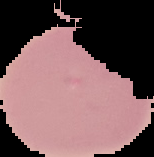
image size = 154×157 pixels
preparation = thin blood film
image type = cell region segmented out of the field of view; surrounding area masked to black
malaria status = uninfected